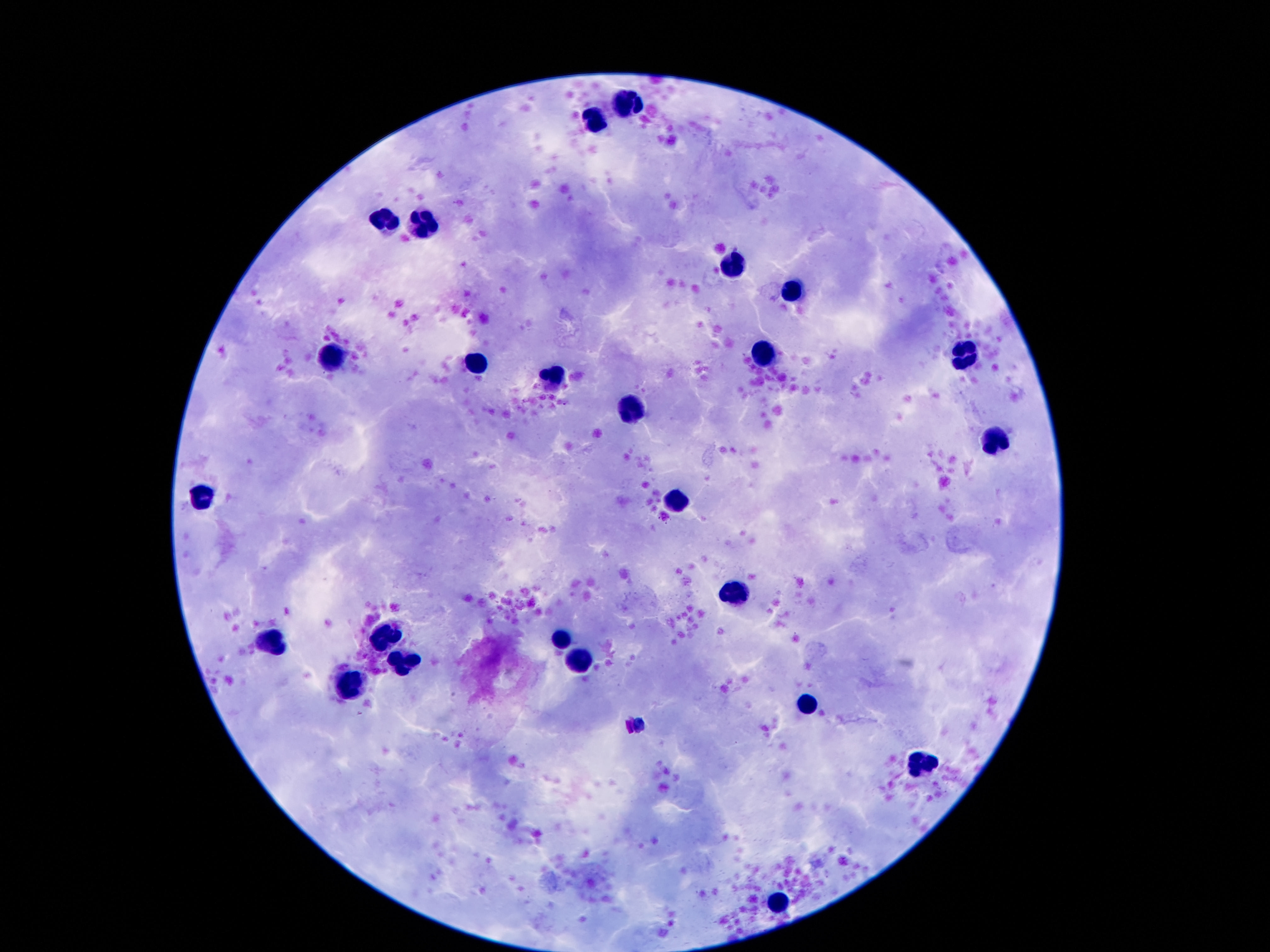
Approximate object centers, in pixels from the top-left corner. Leukocyte locations: (x=631, y=107), (x=597, y=123), (x=384, y=221), (x=425, y=227), (x=734, y=261), (x=791, y=290), (x=967, y=353), (x=766, y=354), (x=332, y=358), (x=474, y=363), (x=554, y=377), (x=633, y=412), (x=994, y=442), (x=203, y=494), (x=678, y=502), (x=734, y=593), (x=386, y=634), (x=560, y=637), (x=271, y=639), (x=582, y=660), (x=402, y=662), (x=349, y=687), (x=805, y=703), (x=926, y=768), (x=775, y=902). Patient malaria status: negative. Giemsa-stained preparation. Smartphone photograph taken through the microscope eyepiece. 100x magnification. Single field of view. Image is 1270×952 pixels. Thick blood film.